Assess this cell for malaria.
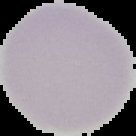
Uninfected.

Cell region segmented out of the field of view; the surrounding area is masked to black. Image is 136×136 pixels. From a thin blood film.